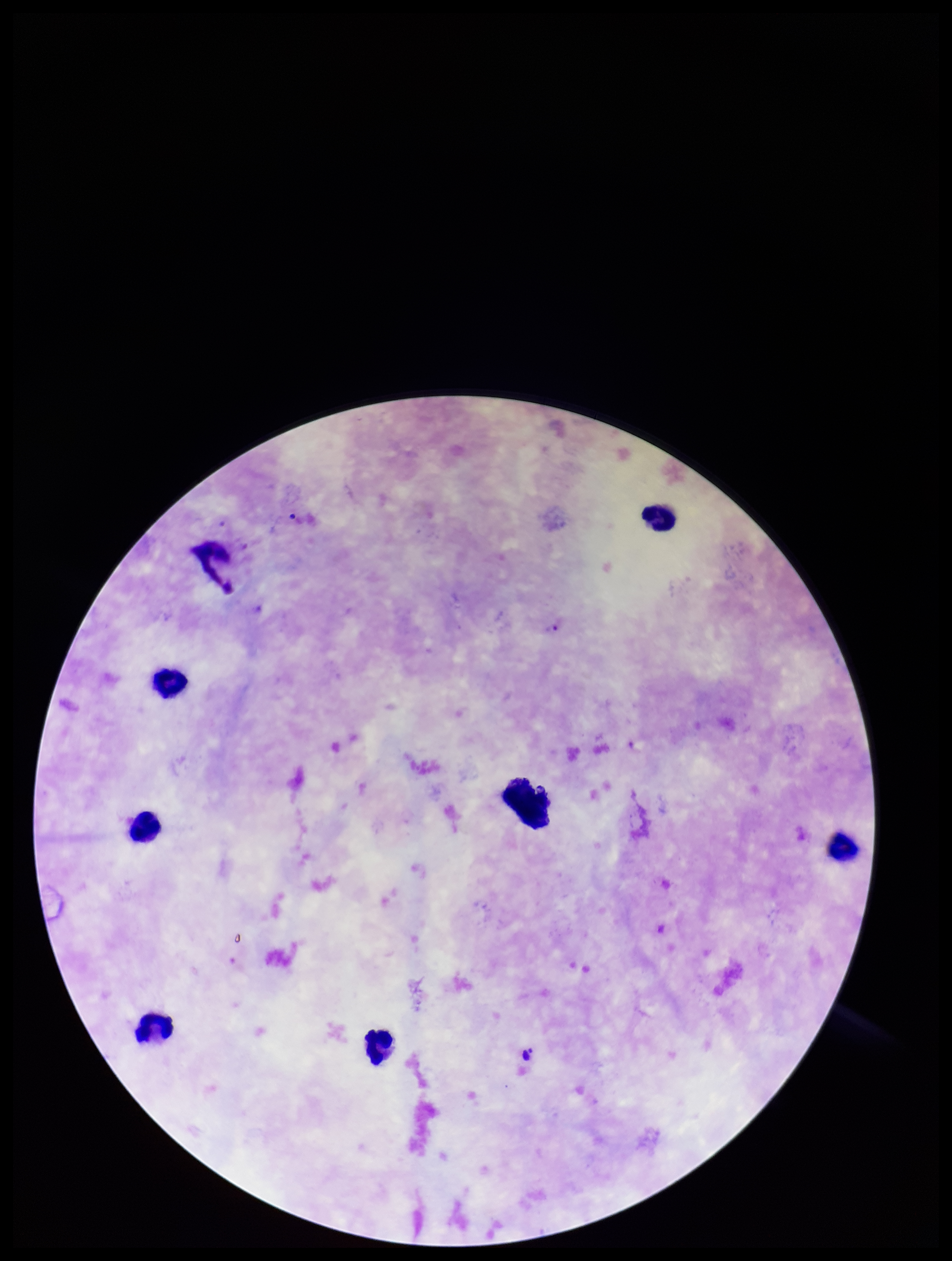
Summary:
  - Plasmodium parasites: seen
  - Parasite count: 2
  - Image size: 952×1261 pixels
  - Stain: Giemsa
  - Species reported for this patient: Plasmodium falciparum
  - Patient malaria status: positive
  - Preparation: thick smear
  - Leukocyte count: 7
  - Capture: smartphone photograph through the microscope eyepiece
  - Field of view: one from this slide